Locate and identify every blood parasite.
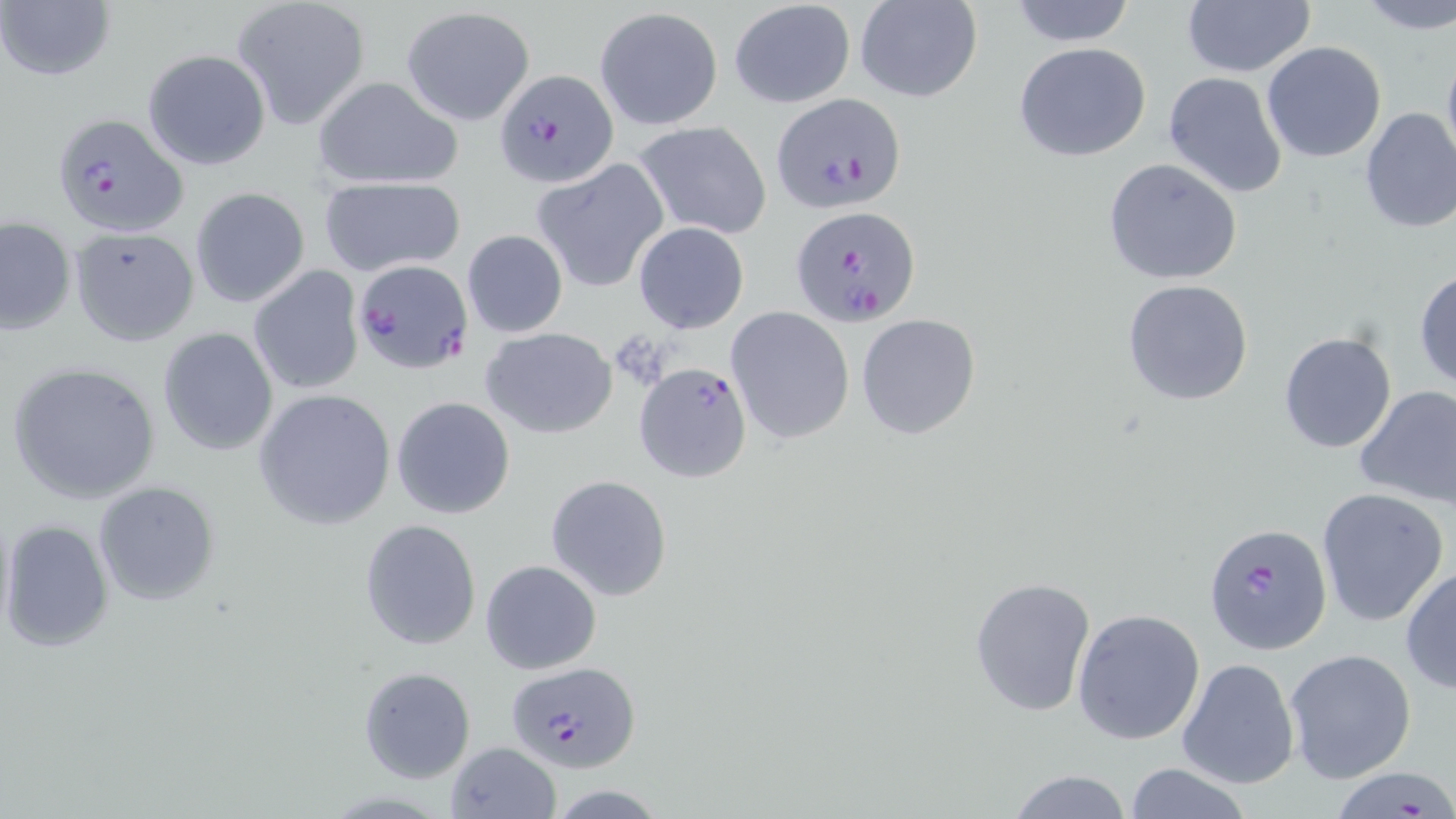

Approximate bounding boxes as (x1, y1, x2, y2) in pixels.
Plasmodium falciparum-infected red blood cells: (495, 68, 618, 186), (771, 91, 907, 214), (51, 111, 189, 238), (789, 204, 921, 326), (349, 260, 475, 373), (632, 361, 752, 483), (1202, 521, 1332, 652), (506, 661, 639, 770), (1334, 763, 1454, 819).
No Plasmodium ovale, Plasmodium malariae, Plasmodium vivax, Babesia divergens, or Trypanosoma brucei observed.

Uninfected red blood cell locations: (231, 0, 370, 129), (1007, 0, 1138, 47), (1355, 0, 1456, 33), (1, 1, 116, 84), (727, 1, 856, 108), (854, 1, 982, 103), (1180, 1, 1316, 78), (400, 6, 535, 125), (595, 7, 723, 130), (1440, 37, 1456, 175), (1261, 41, 1388, 164), (1013, 42, 1154, 163), (141, 48, 271, 170), (1161, 71, 1290, 197), (313, 76, 464, 192), (1356, 106, 1456, 233), (631, 120, 772, 241), (1102, 157, 1243, 285), (533, 158, 668, 293), (319, 178, 466, 276), (190, 187, 309, 308), (1, 217, 76, 336), (632, 221, 750, 334), (68, 227, 199, 346), (462, 230, 567, 338), (248, 266, 366, 396), (1413, 266, 1456, 392), (1122, 278, 1254, 406), (725, 306, 855, 445), (855, 313, 981, 439), (157, 327, 278, 457), (482, 327, 617, 439), (1278, 330, 1399, 454), (8, 361, 160, 506), (1353, 384, 1456, 509), (254, 389, 397, 528), (391, 396, 516, 520), (545, 474, 673, 602), (93, 480, 221, 604), (1316, 487, 1448, 628), (2, 517, 115, 653), (358, 518, 484, 652), (480, 559, 602, 674), (1400, 565, 1456, 694), (969, 576, 1096, 719), (1072, 608, 1205, 744), (1284, 647, 1417, 783), (1178, 657, 1300, 790), (357, 666, 475, 784), (446, 741, 560, 818), (1120, 762, 1252, 819), (1007, 767, 1133, 819). Slide-level diagnosis: Plasmodium falciparum. 1000x magnification. May-Grünwald-Giemsa stain. Thin blood film. Light microscopy. Image is 1456×819 pixels. Single field of view.